Locate every blood parasite and identify its species.
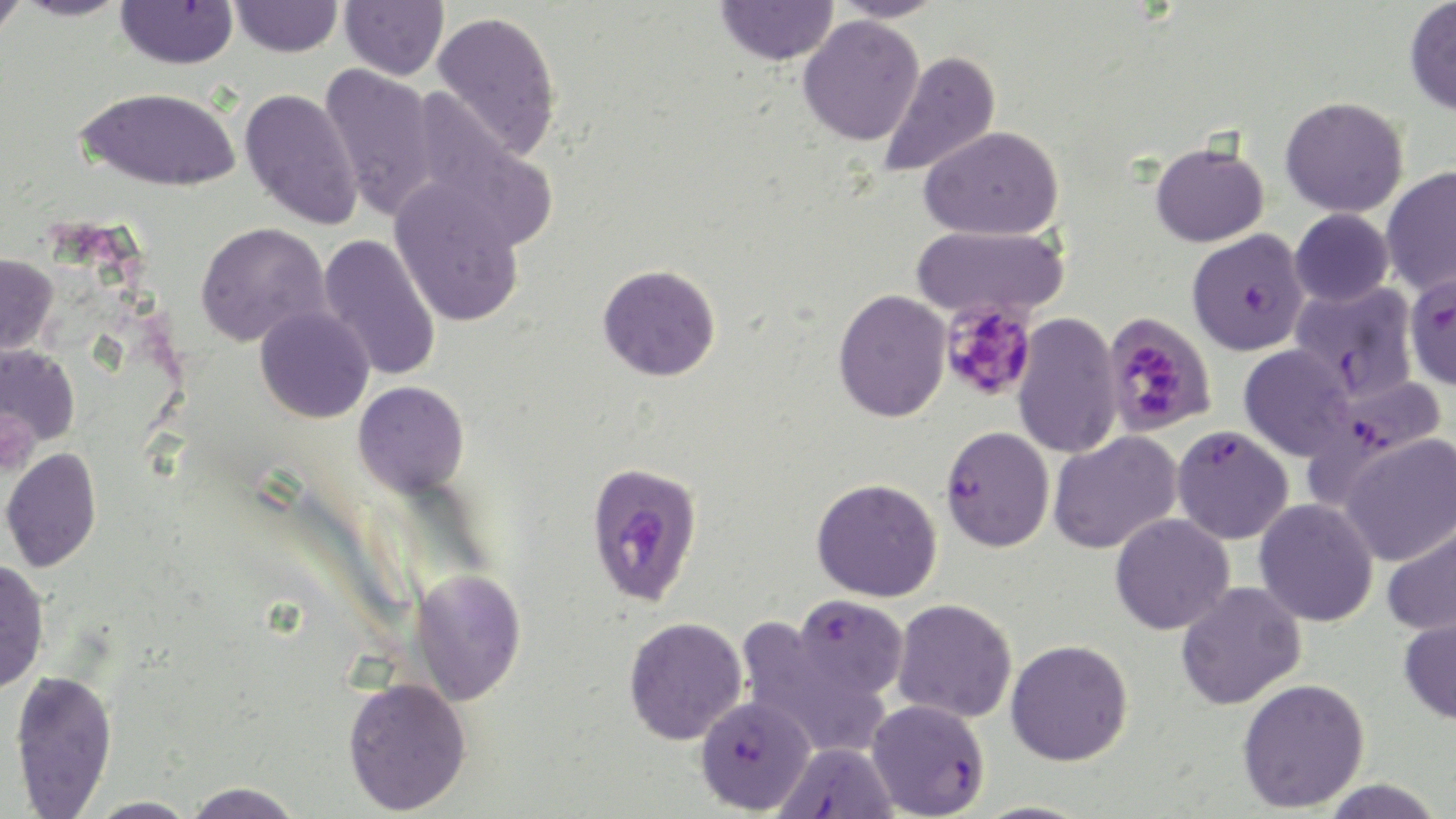
Approximate bounding boxes as [x1, y1, x2, y2] in pixels.
Plasmodium falciparum-infected red blood cells: [1187, 229, 1310, 355], [1404, 272, 1456, 390], [1290, 282, 1419, 403], [1305, 376, 1448, 500], [1171, 425, 1294, 545], [940, 426, 1054, 552], [586, 461, 704, 607], [794, 594, 909, 698], [695, 695, 816, 815], [866, 698, 990, 818], [774, 742, 900, 819].
No Plasmodium ovale, Plasmodium malariae, Plasmodium vivax, Babesia divergens, or Trypanosoma brucei observed.

Uninfected red blood cell locations: [0, 0, 27, 42], [14, 0, 133, 21], [230, 0, 343, 57], [340, 0, 449, 80], [830, 0, 945, 23], [1404, 0, 1456, 116], [116, 1, 239, 69], [716, 1, 838, 66], [431, 10, 562, 160], [798, 16, 925, 146], [880, 50, 1001, 178], [319, 63, 439, 221], [77, 86, 241, 191], [239, 87, 363, 231], [1280, 96, 1408, 217], [410, 101, 558, 251], [920, 125, 1063, 240], [1150, 139, 1269, 248], [1380, 166, 1456, 296], [389, 179, 526, 327], [1290, 208, 1394, 307], [195, 221, 330, 348], [911, 224, 1070, 321], [319, 233, 442, 382], [0, 253, 58, 356], [597, 264, 721, 381], [833, 289, 951, 422], [255, 304, 375, 423], [1012, 312, 1123, 460], [0, 344, 80, 451], [1239, 344, 1354, 461], [354, 381, 469, 497], [1047, 431, 1183, 555], [1338, 433, 1456, 567], [1, 447, 102, 573], [811, 478, 942, 602], [1254, 498, 1379, 627], [1110, 513, 1234, 635], [1382, 515, 1456, 636], [0, 558, 50, 696], [410, 568, 527, 705], [1175, 580, 1306, 709], [892, 598, 1016, 723], [1399, 612, 1456, 725], [624, 617, 747, 744], [735, 617, 889, 761], [1006, 639, 1133, 766], [10, 669, 117, 817], [342, 676, 472, 816], [1237, 677, 1370, 813], [1317, 779, 1446, 818], [185, 782, 304, 818], [87, 796, 199, 818]. Platelet locations: [939, 300, 1039, 403], [0, 409, 39, 476]. Slide-level diagnosis: Plasmodium falciparum. Optical microscopy. May-Grünwald-Giemsa-stained preparation. 1000x magnification. One field of a larger specimen. Image is 1456×819 pixels. Thin blood film.